Classify this cell by malaria status.
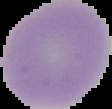
It is uninfected.

image size = 112×109 pixels
preparation = thin blood film
image type = segmented cell region on a black background